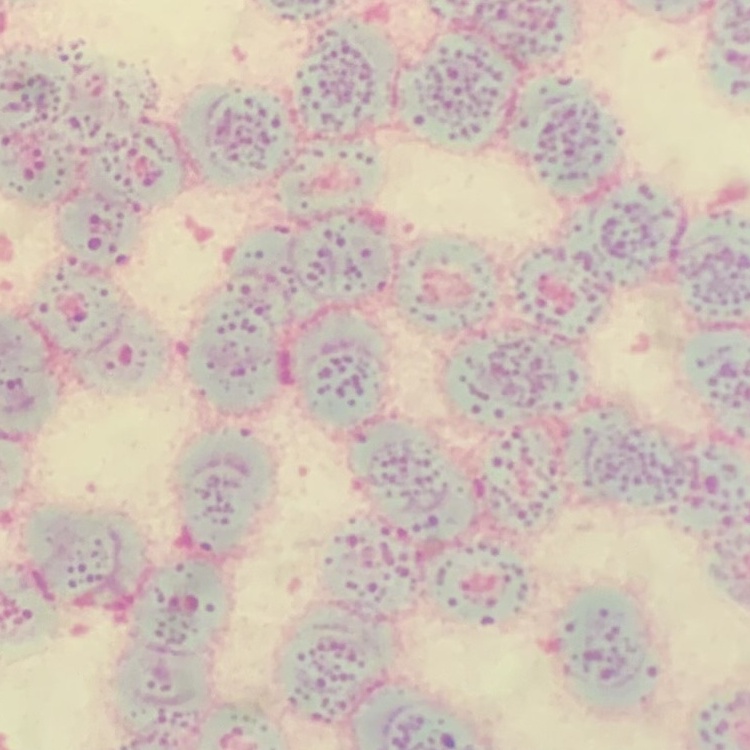

The erythrocytes show rouleaux formation. One tile cut from a larger photomicrograph. Stained with either Field's or Giemsa. Thin blood smear.